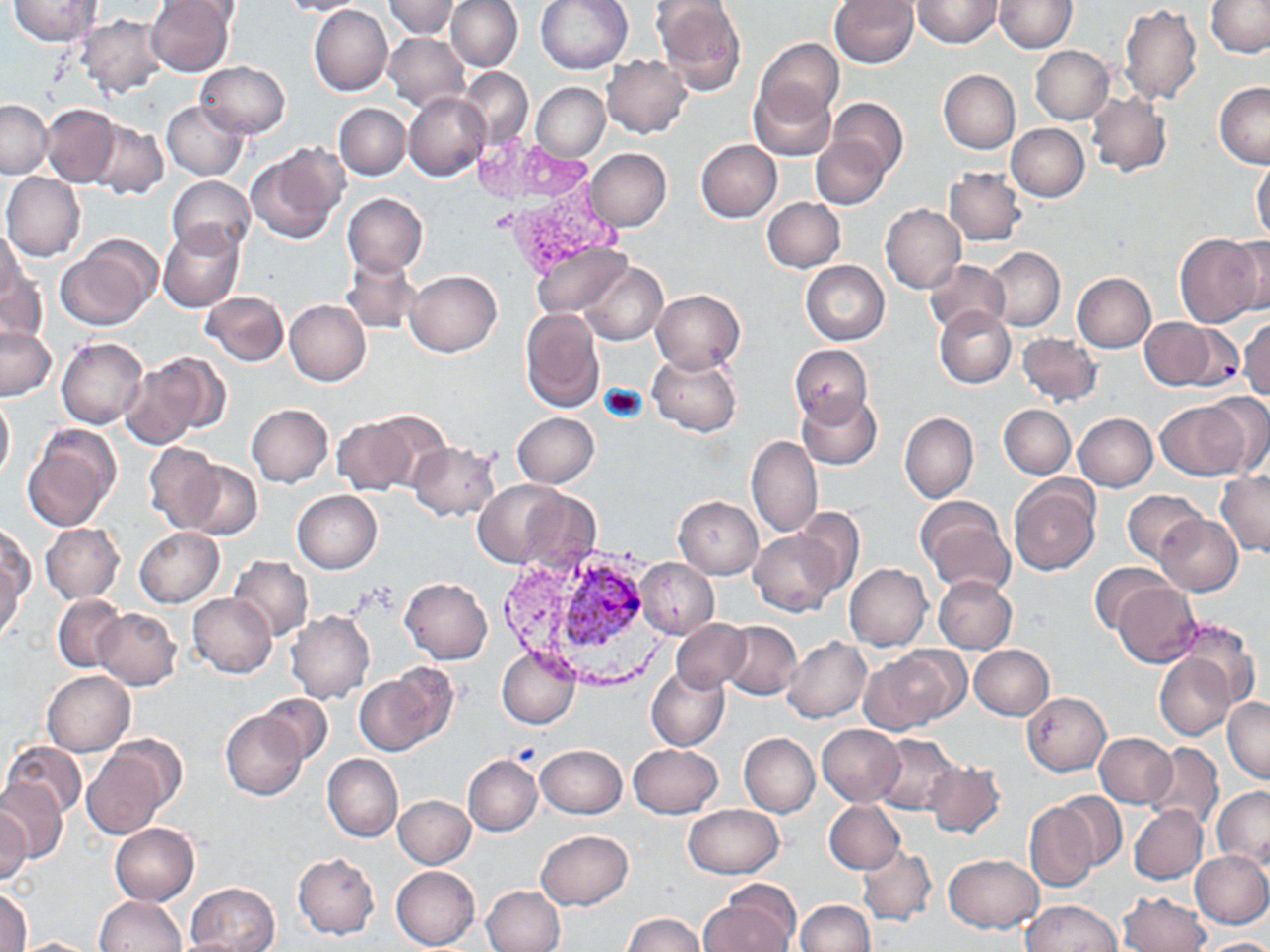

Approximate bounding boxes as (x1,y1)-(x2,y2) corner pairs in pixels. Plasmodium vivax-infected red blood cell locations: (557,564)-(647,657). Uninfected red blood cell locations: (8,0)-(103,46), (146,0)-(236,76), (276,0)-(370,17), (385,0)-(460,38), (446,0)-(523,72), (535,0)-(633,74), (651,0)-(747,95), (831,0)-(919,69), (912,0)-(1002,48), (159,1)-(241,29), (994,1)-(1077,52), (1206,1)-(1270,58), (309,4)-(393,96), (1120,4)-(1202,106), (76,13)-(167,98), (383,32)-(469,111), (756,38)-(843,123), (1029,44)-(1115,124), (601,56)-(692,138), (196,61)-(289,137), (458,69)-(533,146), (939,70)-(1020,153), (1216,82)-(1270,168), (531,83)-(609,161), (748,83)-(835,162), (404,92)-(490,181), (1087,93)-(1171,175), (827,98)-(908,178), (0,99)-(52,177), (162,100)-(248,180), (334,103)-(410,180), (42,104)-(119,187), (93,112)-(246,188), (91,120)-(167,198), (1006,124)-(1089,202), (812,136)-(890,209), (695,139)-(782,222), (248,144)-(347,243), (585,148)-(672,231), (1251,161)-(1270,243), (944,167)-(1025,247), (2,174)-(85,261), (167,175)-(256,256), (342,193)-(428,276), (762,197)-(845,272), (881,205)-(966,294), (158,223)-(244,312), (0,224)-(25,310), (1175,233)-(1266,327), (1223,234)-(1270,318), (56,241)-(158,330), (532,243)-(632,319), (984,248)-(1065,331), (342,254)-(423,332), (924,260)-(1010,336), (800,261)-(890,345), (579,262)-(667,344), (0,263)-(47,348), (404,270)-(501,357), (1073,273)-(1156,352), (651,290)-(744,373), (202,292)-(287,365), (284,300)-(370,385), (933,307)-(1015,389), (520,309)-(605,411), (1140,318)-(1213,390), (1238,318)-(1270,399), (1173,322)-(1243,391), (1,326)-(55,400), (1019,332)-(1102,407), (57,338)-(147,429), (790,343)-(872,425), (648,350)-(742,437), (126,354)-(224,449), (1198,391)-(1270,475), (0,393)-(14,484), (797,394)-(882,470), (1154,400)-(1250,480), (247,404)-(333,487), (999,404)-(1075,478), (512,411)-(599,488), (900,412)-(978,502), (1074,413)-(1157,491), (331,417)-(423,495), (22,425)-(119,531), (746,435)-(823,538), (408,442)-(499,519), (143,443)-(224,532), (180,461)-(262,540), (1215,470)-(1270,557), (473,479)-(567,566), (1010,479)-(1100,577), (508,485)-(603,574), (1122,490)-(1205,563), (292,491)-(382,573), (674,497)-(763,578), (917,497)-(1012,594), (792,508)-(865,593), (1156,514)-(1242,595), (1,524)-(36,604), (41,524)-(124,603), (135,527)-(224,607), (749,527)-(842,617), (228,555)-(313,641), (636,558)-(718,640), (0,559)-(25,646), (844,563)-(932,650), (1088,564)-(1173,635), (933,575)-(1015,653), (400,578)-(492,663), (1112,582)-(1201,668), (187,594)-(276,677), (52,595)-(127,672), (94,608)-(181,690), (287,611)-(373,703), (671,620)-(748,690), (721,621)-(801,700), (782,637)-(871,723), (970,644)-(1053,720), (496,645)-(580,729), (863,648)-(963,732), (1154,652)-(1235,739), (646,666)-(730,750), (355,667)-(453,755), (41,670)-(135,756), (1022,692)-(1110,775), (256,694)-(333,766), (1223,696)-(1269,783), (220,710)-(306,800), (817,723)-(905,806), (740,733)-(819,817), (1093,733)-(1177,808), (103,734)-(188,814), (873,734)-(961,815), (2,740)-(87,819), (1144,741)-(1224,830), (535,744)-(627,817), (629,744)-(722,817), (83,749)-(166,839), (322,754)-(402,842), (463,755)-(541,836), (925,760)-(1004,838), (0,779)-(67,863), (1210,786)-(1270,870), (1053,791)-(1128,872), (392,795)-(475,869), (824,800)-(905,873), (1024,801)-(1098,891), (684,804)-(782,878), (0,805)-(31,887), (1129,805)-(1207,884), (109,822)-(200,906), (536,830)-(632,909), (857,847)-(937,926), (1190,850)-(1270,928), (293,852)-(379,938), (943,854)-(1044,932), (391,866)-(479,950), (186,883)-(278,951), (482,885)-(564,952), (0,887)-(32,951), (702,887)-(801,951), (1119,892)-(1209,952), (94,896)-(186,952), (796,900)-(874,952), (1023,900)-(1121,951), (624,914)-(704,952), (10,938)-(103,951), (1197,938)-(1270,951). Slide-level diagnosis: Plasmodium vivax. May-Grünwald-Giemsa stain. Single field of view. Image is 1270×952 pixels. Thin blood film. Captured at 1000x magnification. Optical microscopy.